Assess this cell for malaria.
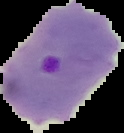
It is parasitized.

preparation: thin blood smear
image_size: 124×133 pixels
image_type: cell region segmented out of the field of view; surrounding area masked to black